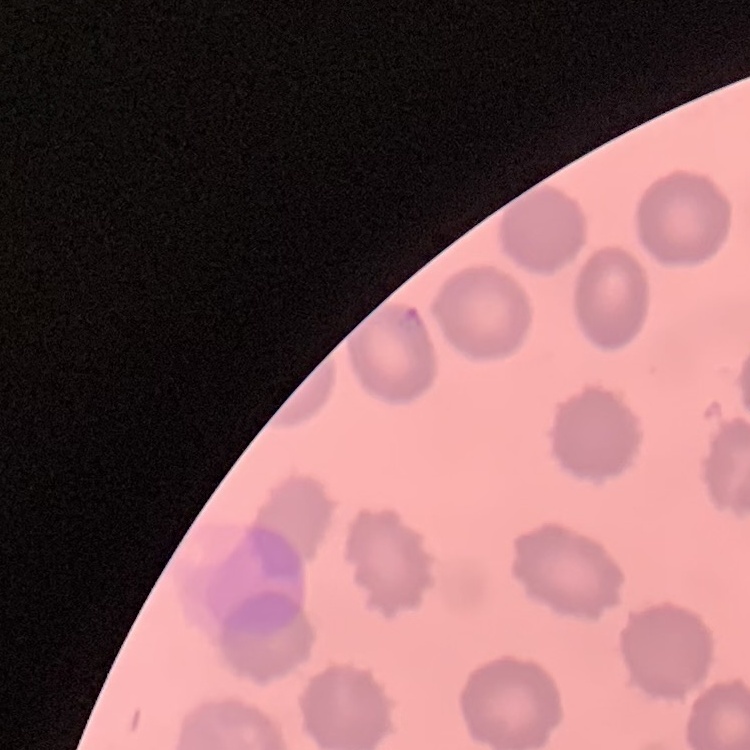

The red blood cells show no rouleaux formation. Stained with either Field's or Giemsa. Thin blood smear. One tile cut from a larger photomicrograph.